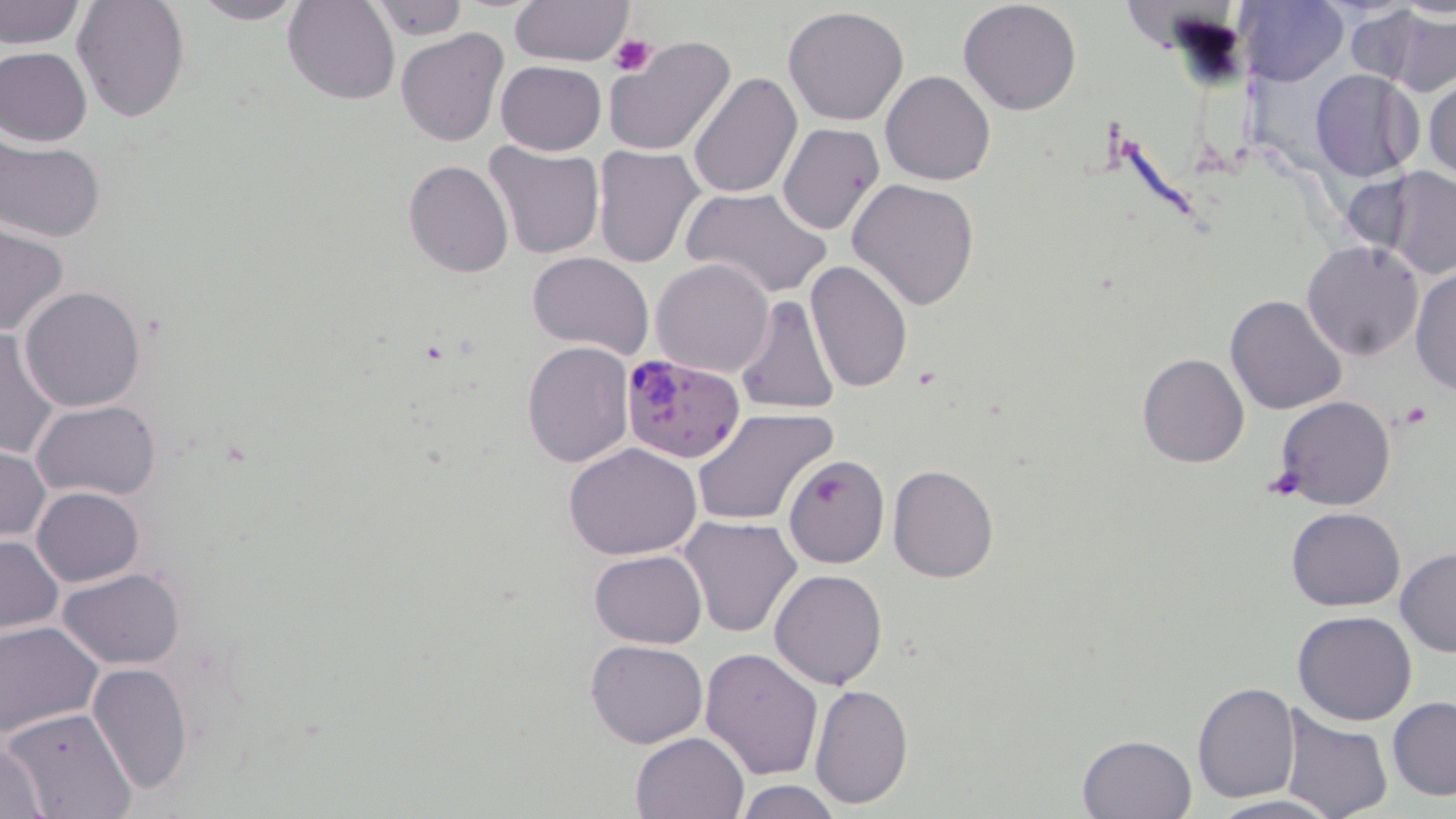
slide-level diagnosis = Plasmodium falciparum
platelet locations = approximate bounding boxes as named x1/y1/x2/y2 corners in pixels: (x1=608, y1=35, x2=655, y2=78)
field of view = one of a larger specimen
modality = light microscopy
stain = May-Grünwald-Giemsa
preparation = thin blood film
image size = 1456×819 pixels
Plasmodium falciparum-infected red blood cell locations = approximate bounding boxes as named x1/y1/x2/y2 corners in pixels: (x1=618, y1=354, x2=745, y2=462)
uninfected red blood cell locations = approximate bounding boxes as named x1/y1/x2/y2 corners in pixels: (x1=0, y1=0, x2=85, y2=51), (x1=73, y1=0, x2=191, y2=121), (x1=283, y1=0, x2=399, y2=104), (x1=366, y1=0, x2=470, y2=42), (x1=509, y1=0, x2=634, y2=68), (x1=186, y1=1, x2=310, y2=25), (x1=1236, y1=1, x2=1349, y2=86), (x1=958, y1=2, x2=1082, y2=115), (x1=783, y1=6, x2=910, y2=127), (x1=1355, y1=6, x2=1453, y2=95), (x1=395, y1=28, x2=507, y2=146), (x1=604, y1=34, x2=737, y2=158), (x1=0, y1=46, x2=92, y2=148), (x1=496, y1=61, x2=605, y2=155), (x1=881, y1=70, x2=996, y2=186), (x1=1311, y1=70, x2=1423, y2=181), (x1=688, y1=72, x2=802, y2=200), (x1=1424, y1=73, x2=1456, y2=185), (x1=777, y1=122, x2=884, y2=235), (x1=1, y1=139, x2=105, y2=242), (x1=481, y1=141, x2=604, y2=261), (x1=592, y1=145, x2=706, y2=267), (x1=403, y1=159, x2=515, y2=278), (x1=1381, y1=165, x2=1456, y2=279), (x1=1341, y1=169, x2=1435, y2=267), (x1=848, y1=178, x2=980, y2=311), (x1=681, y1=186, x2=832, y2=299), (x1=0, y1=226, x2=69, y2=337), (x1=1302, y1=240, x2=1424, y2=361), (x1=527, y1=251, x2=654, y2=359), (x1=651, y1=258, x2=776, y2=379), (x1=805, y1=259, x2=915, y2=395), (x1=1409, y1=265, x2=1456, y2=393), (x1=19, y1=286, x2=147, y2=411), (x1=1226, y1=294, x2=1346, y2=414), (x1=735, y1=296, x2=840, y2=417), (x1=0, y1=330, x2=64, y2=459), (x1=522, y1=341, x2=633, y2=467), (x1=1137, y1=353, x2=1250, y2=469), (x1=1275, y1=396, x2=1396, y2=510), (x1=32, y1=399, x2=161, y2=500), (x1=691, y1=408, x2=835, y2=527), (x1=564, y1=443, x2=703, y2=560), (x1=0, y1=444, x2=48, y2=542), (x1=784, y1=454, x2=889, y2=569), (x1=888, y1=465, x2=999, y2=583), (x1=32, y1=486, x2=144, y2=586), (x1=1286, y1=506, x2=1406, y2=611), (x1=678, y1=516, x2=804, y2=639), (x1=1, y1=534, x2=62, y2=633), (x1=589, y1=548, x2=707, y2=648), (x1=1395, y1=548, x2=1456, y2=657), (x1=59, y1=569, x2=185, y2=669), (x1=770, y1=569, x2=888, y2=691), (x1=1294, y1=611, x2=1417, y2=726), (x1=0, y1=621, x2=102, y2=738), (x1=586, y1=639, x2=707, y2=747), (x1=699, y1=646, x2=822, y2=780), (x1=86, y1=661, x2=196, y2=797), (x1=808, y1=681, x2=913, y2=808), (x1=1192, y1=683, x2=1300, y2=803), (x1=1387, y1=696, x2=1456, y2=800), (x1=1, y1=706, x2=138, y2=819), (x1=1279, y1=706, x2=1393, y2=819), (x1=631, y1=732, x2=747, y2=819), (x1=1077, y1=733, x2=1198, y2=819), (x1=1, y1=736, x2=54, y2=817), (x1=733, y1=779, x2=842, y2=819), (x1=1205, y1=793, x2=1343, y2=819)
magnification = 1000x